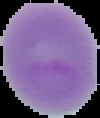

Summary:
  - Malaria status: uninfected
  - Image type: segmented cell region on a black background
  - Preparation: thin blood smear
  - Image size: 100×118 pixels